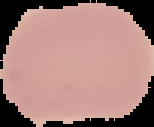

image type = segmented cell region on a black background
result = no Plasmodium parasites detected
preparation = thin blood film
image size = 154×127 pixels